Give the preparation type.
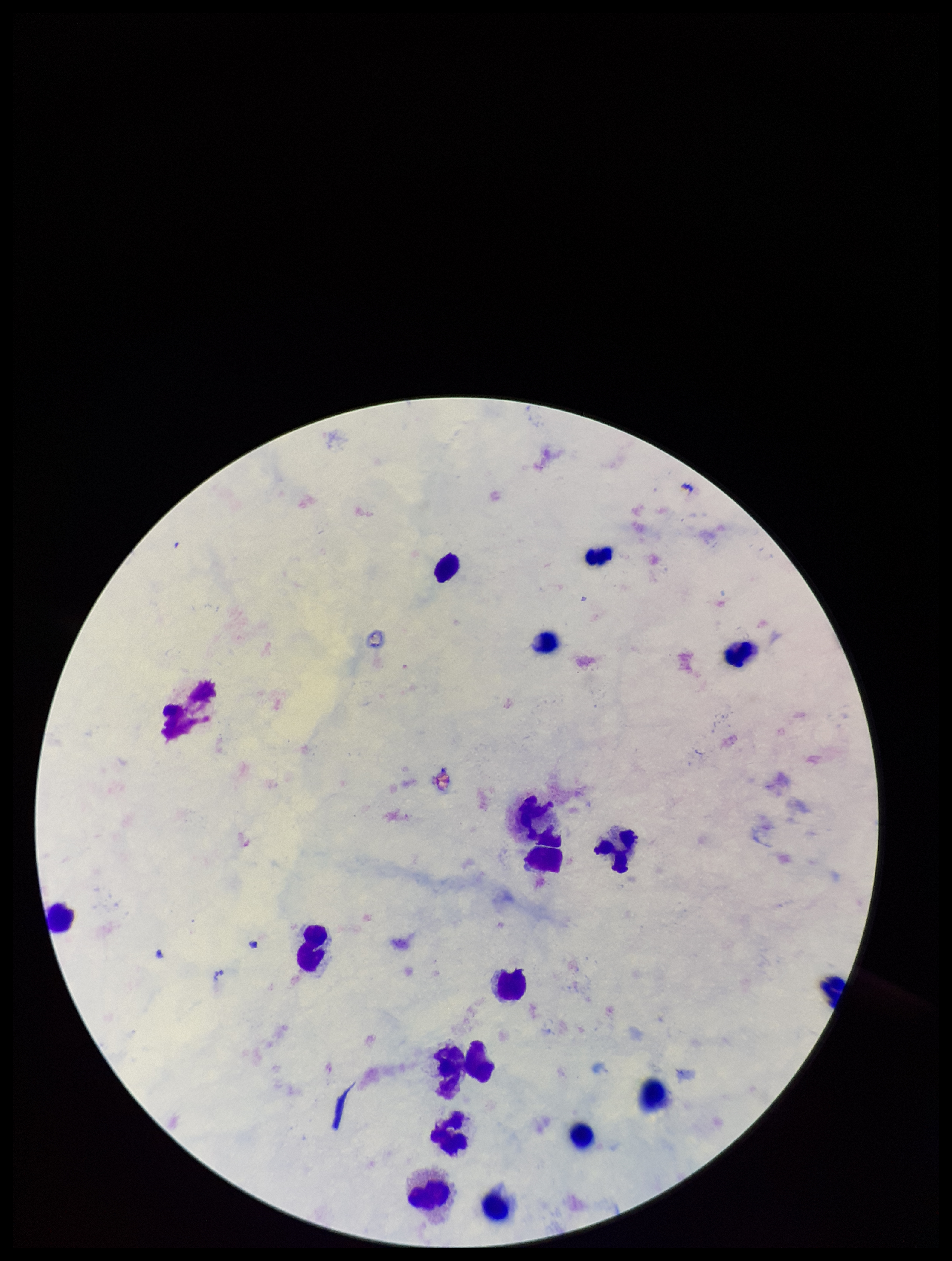
It is a thick blood smear.

patient malaria status = infected
image size = 952×1261 pixels
leukocyte count = 18
species reported for this patient = Plasmodium falciparum
capture = smartphone photograph through the microscope eyepiece
stain = Giemsa
field of view = one from this slide
parasite count = 0
Plasmodium parasites = none detected